Classify this cell by malaria status.
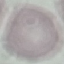
It is uninfected.

Summary:
  - Preparation: thin blood smear
  - Stain: Giemsa
  - Capture: smartphone through the microscope eyepiece
  - Image type: automatically extracted cell patch, resized to 64 × 64 pixels